Report the malaria status of this cell.
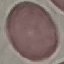
It is uninfected.

capture = smartphone through the microscope eyepiece
image type = automatically extracted cell patch, resized to 64 × 64 pixels
preparation = thin blood film
stain = Giemsa